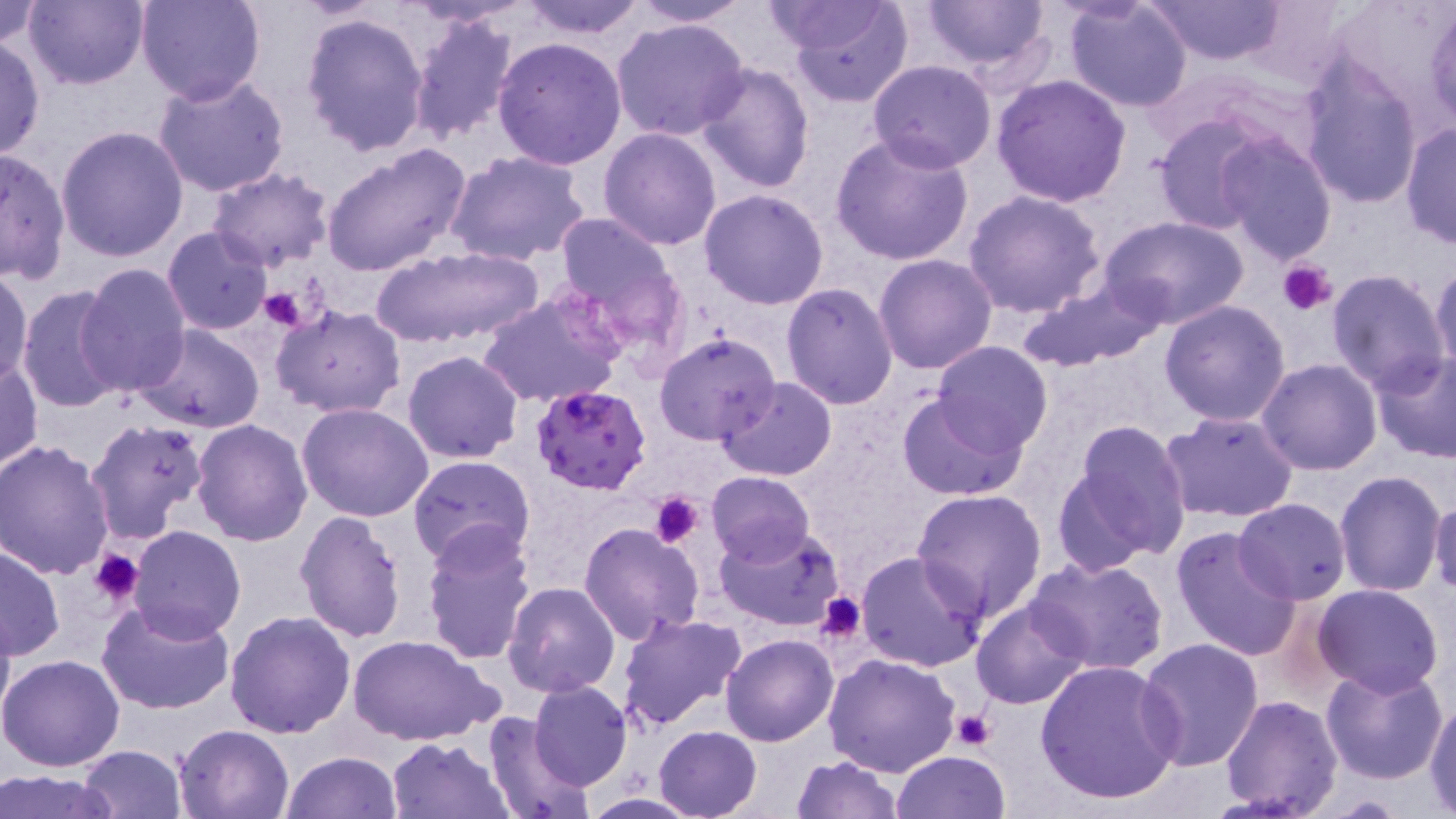

Approximate bounding boxes as (x1, y1, x2, y2) in pixels. Plasmodium falciparum-infected red blood cell locations: (531, 385, 651, 495). Platelet locations: (1280, 260, 1335, 316), (259, 285, 311, 332), (651, 491, 704, 547), (88, 548, 144, 606), (816, 591, 869, 643), (950, 710, 994, 751). Uninfected red blood cell locations: (23, 0, 147, 90), (136, 0, 265, 105), (517, 0, 649, 39), (627, 0, 754, 25), (785, 0, 914, 107), (919, 0, 1054, 73), (1148, 0, 1284, 64), (1239, 0, 1359, 89), (764, 1, 895, 55), (1063, 1, 1194, 112), (1, 2, 43, 49), (1427, 5, 1456, 130), (299, 12, 431, 157), (408, 14, 519, 144), (610, 17, 750, 142), (0, 35, 44, 160), (494, 38, 627, 171), (1297, 58, 1426, 207), (869, 59, 996, 172), (696, 63, 814, 193), (152, 73, 290, 197), (990, 76, 1133, 209), (1152, 113, 1274, 234), (1401, 121, 1455, 248), (56, 126, 190, 264), (599, 127, 723, 249), (827, 131, 974, 267), (1215, 133, 1340, 264), (321, 143, 472, 277), (0, 148, 70, 282), (445, 151, 590, 265), (207, 167, 335, 272), (699, 188, 830, 310), (962, 190, 1107, 318), (550, 215, 679, 335), (1103, 217, 1247, 330), (162, 227, 272, 336), (369, 244, 546, 348), (874, 253, 998, 374), (1429, 258, 1456, 379), (75, 262, 192, 397), (1, 267, 34, 388), (1327, 268, 1453, 395), (1015, 280, 1163, 371), (781, 282, 898, 409), (16, 285, 126, 414), (477, 294, 621, 408), (1160, 298, 1291, 425), (272, 306, 406, 418), (135, 326, 266, 433), (654, 331, 780, 444), (932, 341, 1054, 455), (402, 349, 523, 463), (1369, 350, 1456, 463), (1, 357, 43, 474), (1257, 359, 1383, 475), (714, 376, 838, 480), (896, 391, 1026, 500), (297, 401, 434, 522), (1159, 410, 1299, 524), (85, 416, 211, 545), (189, 419, 313, 546), (1062, 419, 1194, 565), (1, 439, 117, 579), (407, 455, 533, 569), (1335, 470, 1446, 596), (705, 472, 815, 566), (912, 488, 1047, 624), (1429, 495, 1456, 599), (1233, 497, 1353, 604), (294, 511, 409, 646), (579, 521, 705, 646), (420, 524, 537, 667), (714, 525, 843, 632), (1171, 525, 1302, 661), (130, 527, 246, 643), (1, 543, 65, 661), (856, 551, 986, 673), (1027, 556, 1170, 676), (502, 583, 620, 698), (1311, 584, 1444, 698), (503, 598, 741, 715), (97, 599, 236, 717), (0, 600, 17, 728), (971, 600, 1089, 710), (224, 610, 356, 738), (617, 612, 745, 733), (720, 634, 838, 747), (349, 635, 498, 748), (1134, 638, 1264, 773), (824, 652, 960, 775), (0, 653, 127, 773), (1034, 658, 1184, 806), (1320, 665, 1449, 785), (529, 681, 633, 790), (1220, 695, 1344, 818), (1426, 702, 1456, 814), (482, 710, 595, 819), (173, 724, 295, 818), (655, 725, 763, 818), (386, 736, 513, 818), (76, 745, 187, 819), (891, 750, 1013, 817), (280, 751, 401, 819), (790, 755, 904, 818), (1, 771, 120, 819), (577, 792, 706, 818). Slide-level diagnosis: Plasmodium falciparum. Thin blood smear. Single field of view. Light microscopy. May-Grünwald-Giemsa stain. 1000x magnification. Image is 1456×819 pixels.